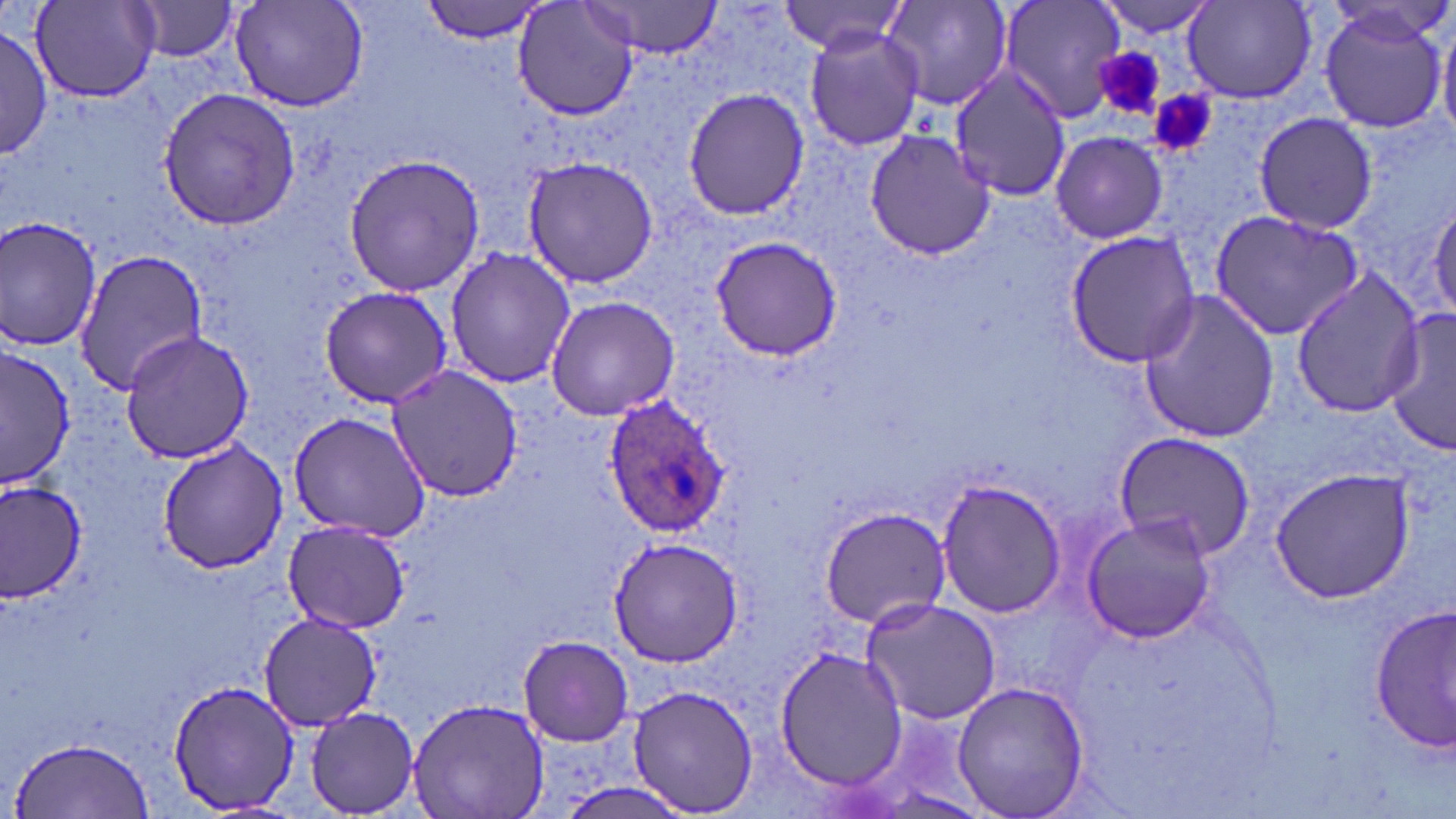 Approximate bounding boxes as named x1/y1/x2/y2 corners in pixels. Plasmodium ovale-infected red blood cell locations: (x1=602, y1=396, x2=731, y2=540). Platelet locations: (x1=1095, y1=48, x2=1166, y2=117), (x1=1152, y1=93, x2=1216, y2=158). Uninfected red blood cell locations: (x1=422, y1=0, x2=550, y2=42), (x1=514, y1=0, x2=640, y2=122), (x1=880, y1=0, x2=1013, y2=113), (x1=997, y1=0, x2=1127, y2=121), (x1=1093, y1=0, x2=1220, y2=36), (x1=30, y1=1, x2=162, y2=101), (x1=130, y1=1, x2=239, y2=63), (x1=782, y1=1, x2=910, y2=56), (x1=230, y1=2, x2=368, y2=111), (x1=582, y1=2, x2=724, y2=58), (x1=1181, y1=2, x2=1317, y2=104), (x1=1316, y1=3, x2=1451, y2=135), (x1=1436, y1=10, x2=1456, y2=143), (x1=804, y1=25, x2=923, y2=153), (x1=0, y1=28, x2=51, y2=161), (x1=948, y1=66, x2=1071, y2=200), (x1=157, y1=88, x2=301, y2=231), (x1=682, y1=89, x2=809, y2=220), (x1=1252, y1=113, x2=1380, y2=233), (x1=864, y1=130, x2=994, y2=261), (x1=1050, y1=131, x2=1169, y2=242), (x1=343, y1=153, x2=486, y2=296), (x1=522, y1=156, x2=663, y2=288), (x1=1429, y1=192, x2=1456, y2=322), (x1=1210, y1=208, x2=1365, y2=341), (x1=0, y1=214, x2=103, y2=355), (x1=1066, y1=231, x2=1202, y2=368), (x1=708, y1=235, x2=844, y2=360), (x1=445, y1=246, x2=576, y2=389), (x1=74, y1=247, x2=206, y2=396), (x1=1288, y1=268, x2=1426, y2=418), (x1=318, y1=285, x2=455, y2=408), (x1=1139, y1=287, x2=1282, y2=443), (x1=545, y1=294, x2=679, y2=421), (x1=1386, y1=306, x2=1456, y2=459), (x1=120, y1=330, x2=256, y2=465), (x1=0, y1=347, x2=75, y2=491), (x1=385, y1=363, x2=523, y2=504), (x1=285, y1=411, x2=431, y2=542), (x1=1111, y1=433, x2=1254, y2=558), (x1=156, y1=441, x2=291, y2=573), (x1=1267, y1=466, x2=1417, y2=603), (x1=1, y1=477, x2=85, y2=602), (x1=936, y1=477, x2=1067, y2=619), (x1=816, y1=505, x2=952, y2=628), (x1=1080, y1=514, x2=1218, y2=644), (x1=283, y1=519, x2=409, y2=634), (x1=606, y1=537, x2=746, y2=666), (x1=859, y1=597, x2=1003, y2=725), (x1=1371, y1=605, x2=1455, y2=754), (x1=258, y1=612, x2=381, y2=731), (x1=519, y1=635, x2=633, y2=744), (x1=775, y1=644, x2=909, y2=791), (x1=166, y1=678, x2=299, y2=815), (x1=951, y1=680, x2=1091, y2=819), (x1=626, y1=684, x2=762, y2=816), (x1=405, y1=697, x2=551, y2=819), (x1=304, y1=706, x2=423, y2=816), (x1=11, y1=735, x2=154, y2=817). Slide-level diagnosis: Plasmodium ovale. May-Grünwald-Giemsa-stained preparation. 1000x magnification. Light microscopy. Thin blood smear. Single field of view. Image is 1456×819 pixels.